Locate every Plasmodium parasite and every leukocyte.
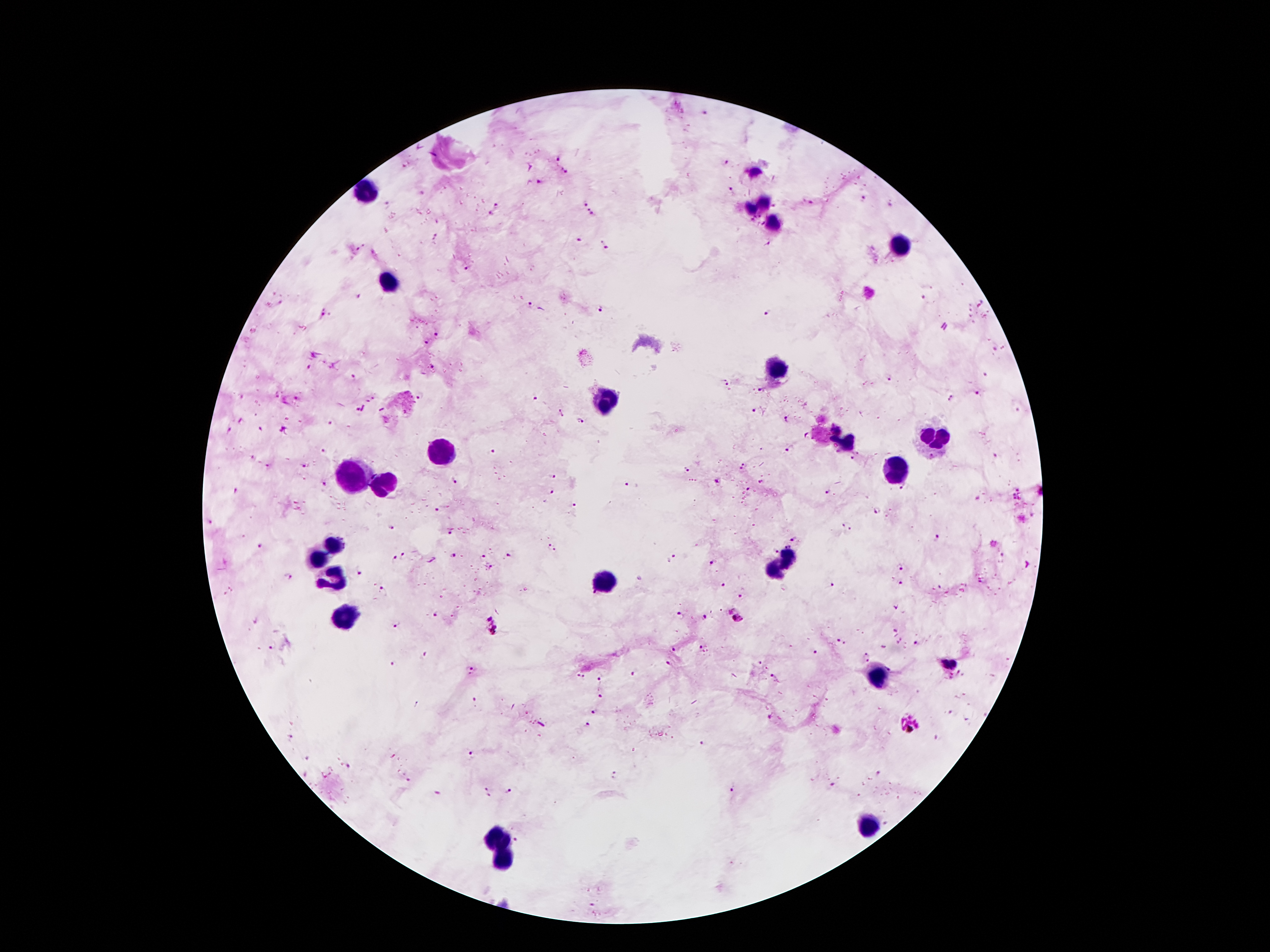

Approximate centers as [x, y] in pixels.
Plasmodium parasites: [707, 113], [558, 159], [726, 163], [404, 166], [564, 170], [539, 182], [732, 188], [422, 193], [863, 199], [585, 202], [810, 202], [387, 204], [497, 205], [590, 212], [491, 214], [578, 240], [604, 244], [466, 268], [924, 297], [530, 306], [601, 309], [768, 312], [323, 315], [439, 334], [428, 342], [994, 349], [309, 368], [984, 375], [355, 377], [889, 377], [725, 383], [760, 391], [977, 394], [420, 396], [536, 398], [950, 398], [754, 410], [560, 413], [787, 420], [583, 421], [333, 424], [228, 431], [806, 434], [491, 450], [791, 450], [323, 453], [858, 453], [995, 457], [851, 460], [744, 465], [304, 466], [688, 469], [453, 479], [550, 479], [718, 481], [761, 483], [626, 484], [324, 485], [748, 488], [828, 491], [552, 492], [1017, 494], [977, 497], [572, 506], [437, 509], [879, 511], [210, 522], [848, 526], [390, 528], [450, 531], [936, 537], [795, 540], [787, 544], [994, 544], [259, 546], [552, 548], [777, 552], [404, 555], [510, 555], [481, 556], [672, 556], [454, 557], [394, 559], [711, 562], [899, 566], [490, 568], [358, 572], [288, 576], [723, 584], [832, 585], [902, 585], [941, 586], [383, 590], [593, 594], [739, 595], [895, 609], [437, 614], [682, 615], [705, 617], [737, 617], [256, 621], [397, 624], [493, 627], [895, 630], [899, 639], [841, 641], [916, 642], [270, 646], [703, 647], [673, 649], [814, 653], [423, 655], [866, 656], [950, 662], [396, 663], [669, 663], [471, 671], [635, 673], [959, 674], [579, 677], [951, 677], [599, 678], [773, 678], [599, 696], [474, 701], [594, 712], [772, 717], [909, 723], [588, 725], [291, 737], [702, 744], [473, 756], [308, 757], [349, 765], [615, 775], [408, 780], [830, 784], [732, 789], [509, 792], [436, 793], [487, 793], [516, 840].
Leukocytes: [754, 171], [366, 194], [766, 203], [752, 209], [774, 225], [900, 248], [392, 282], [778, 366], [606, 401], [935, 437], [846, 442], [442, 453], [894, 470], [351, 480], [385, 488], [335, 545], [320, 559], [781, 565], [335, 577], [600, 584], [344, 610], [878, 679], [867, 827], [493, 835], [504, 857].

100x magnification. Giemsa stain. Smartphone photograph taken through the microscope eyepiece. One field from this slide. Thick peripheral-blood smear. Image is 1270×952 pixels. Patient malaria status: positive for Plasmodium falciparum.